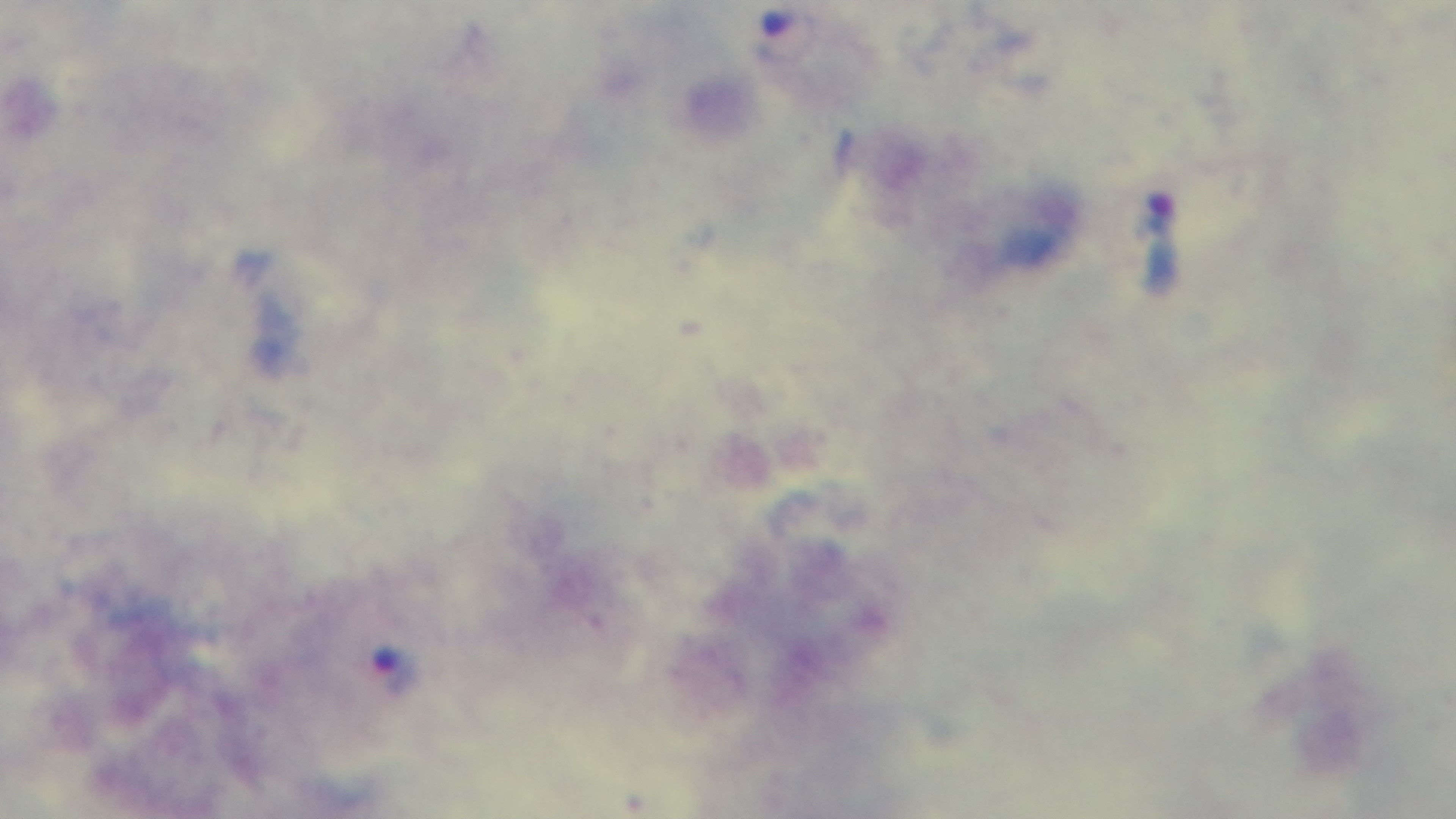 Preparation: thick. Oil-immersion objective, 100x. Light microscopy. Malaria status: infected. Single field of view. Mounted 4K digital camera. Giemsa-stained.